Assess this cell for malaria.
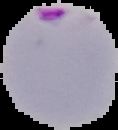
Parasitized.

preparation = thin blood film
image type = cell region segmented out of the field of view; surrounding area masked to black
image size = 118×130 pixels